Classify this cell by malaria status.
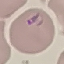

Parasitized.

Giemsa-stained preparation. Thin blood film. Photographed with a smartphone camera at the microscope eyepiece. Cell patch, automatically extracted from a larger field of view and resized to 64 × 64 pixels.